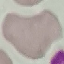

result = no malaria parasites seen
preparation = thin blood film
capture = smartphone camera at the microscope eyepiece
stain = Giemsa
image type = cell patch, automatically extracted from a larger field of view and resized to 64 × 64 pixels